Outline each blood parasite and name the species.
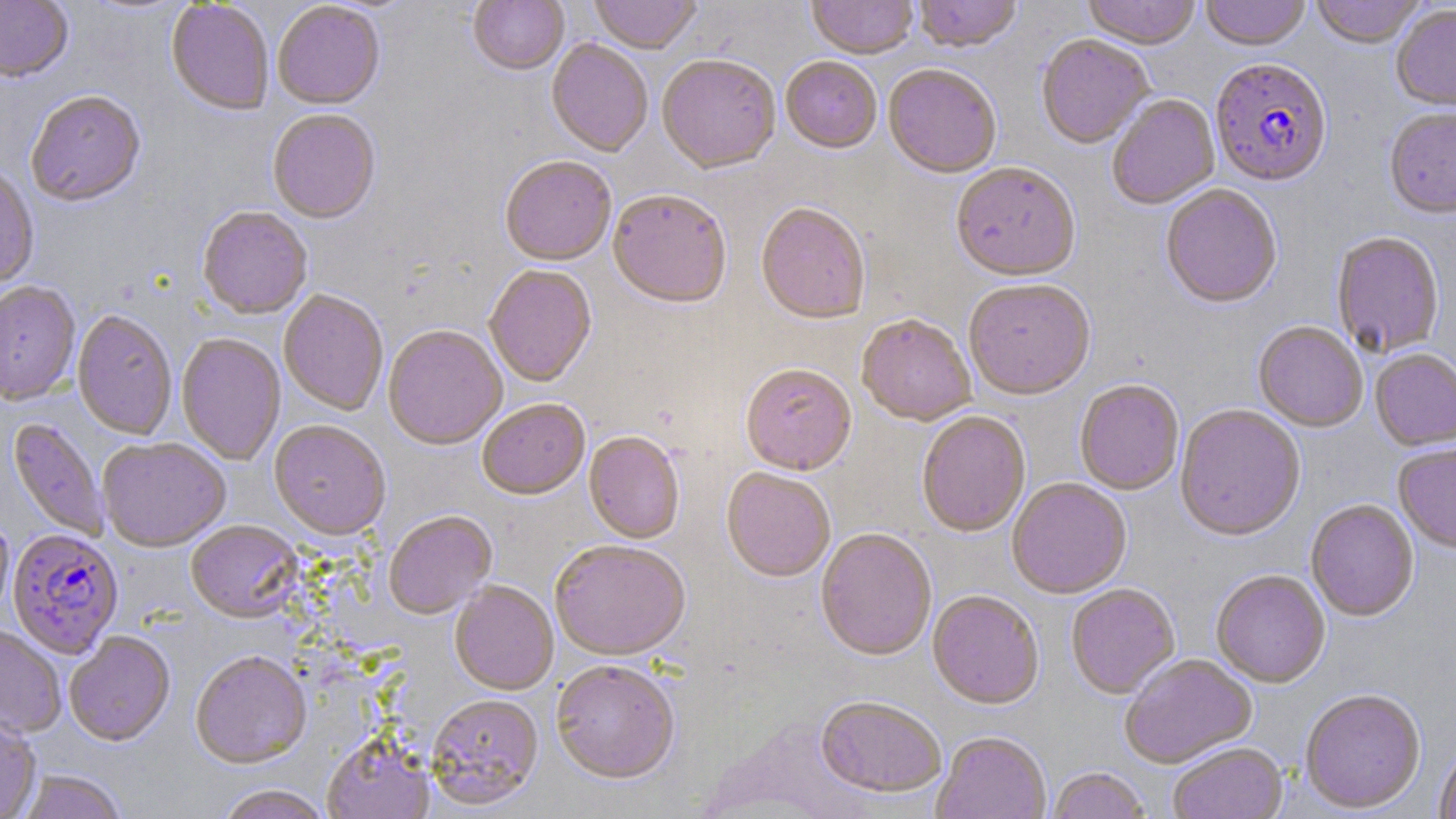

Approximate bounding boxes as (x1,y1)-(x2,y2) corner pairs in pixels.
Plasmodium falciparum-infected red blood cells: (1209,60)-(1333,190), (7,531)-(123,660).
No Plasmodium ovale, Plasmodium malariae, Plasmodium vivax, Babesia divergens, or Trypanosoma brucei observed.

Summary:
  - Uninfected red blood cell locations: (0,0)-(73,85), (468,0)-(569,77), (590,0)-(701,56), (807,0)-(918,61), (914,0)-(1022,55), (1082,0)-(1201,52), (1200,0)-(1311,53), (1310,0)-(1427,50), (165,2)-(274,117), (273,3)-(385,112), (1391,5)-(1456,114), (1036,36)-(1154,150), (546,40)-(653,159), (657,57)-(780,177), (780,58)-(882,156), (883,67)-(1001,180), (26,93)-(146,209), (1108,95)-(1221,210), (1384,109)-(1456,221), (267,111)-(380,226), (499,158)-(616,268), (951,164)-(1081,284), (0,168)-(39,291), (1161,186)-(1282,311), (607,191)-(731,312), (755,205)-(870,327), (196,208)-(312,320), (1331,233)-(1445,359), (484,267)-(597,388), (964,281)-(1096,403), (0,282)-(80,405), (279,290)-(389,416), (72,311)-(177,441), (856,316)-(976,428), (1253,323)-(1367,433), (383,327)-(507,452), (176,334)-(286,466), (1370,350)-(1456,452), (740,366)-(856,478), (1075,381)-(1184,497), (477,401)-(590,502), (1175,405)-(1306,544), (916,413)-(1031,539), (6,419)-(109,542), (269,422)-(391,543), (584,433)-(685,545), (98,439)-(230,554), (1394,444)-(1456,556), (721,469)-(834,584), (1007,480)-(1131,600), (1305,500)-(1419,624), (383,512)-(497,621), (0,515)-(13,622), (186,521)-(304,625), (816,530)-(936,663), (550,543)-(690,664), (1211,572)-(1330,689), (450,582)-(558,697), (1066,584)-(1180,700), (927,591)-(1044,712), (0,626)-(66,738), (65,634)-(176,747), (191,653)-(312,771), (1120,655)-(1258,770), (551,662)-(680,786), (1300,691)-(1427,815), (426,696)-(544,812), (815,698)-(946,800), (0,715)-(41,819), (932,733)-(1051,819), (323,735)-(434,819), (1434,742)-(1456,819), (1169,744)-(1288,819), (1047,768)-(1150,819), (17,771)-(127,819), (216,786)-(331,819)
  - Slide-level diagnosis: Plasmodium falciparum
  - Field of view: single
  - Preparation: thin blood smear
  - Image size: 1456×819 pixels
  - Stain: May-Grünwald-Giemsa
  - Magnification: 1000x
  - Modality: light microscopy